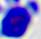
identification = leukocyte
modality = micrograph
magnification = 400x